Comment on the morphology of the erythrocytes.
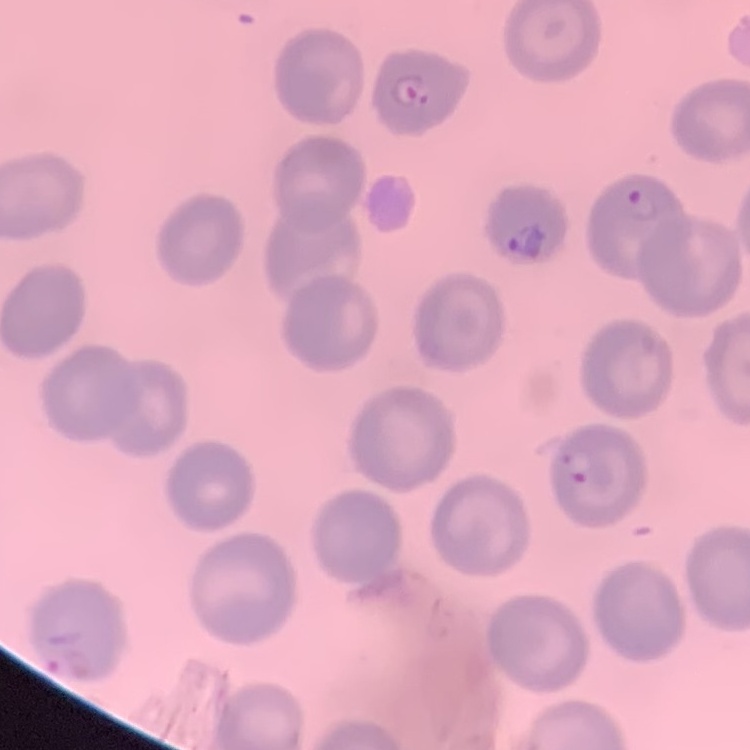
No rouleaux formation.

Summary:
  - Image type: square crop of a larger photomicrograph
  - Preparation: thin peripheral smear
  - Stain: Field's or Giemsa